Report the malaria status of this cell.
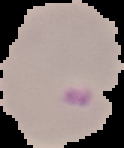
Parasitized.

Image is 124×148 pixels. Cell region segmented out of the field of view; the surrounding area is masked to black. From a thin blood film.